Locate every Plasmodium parasite.
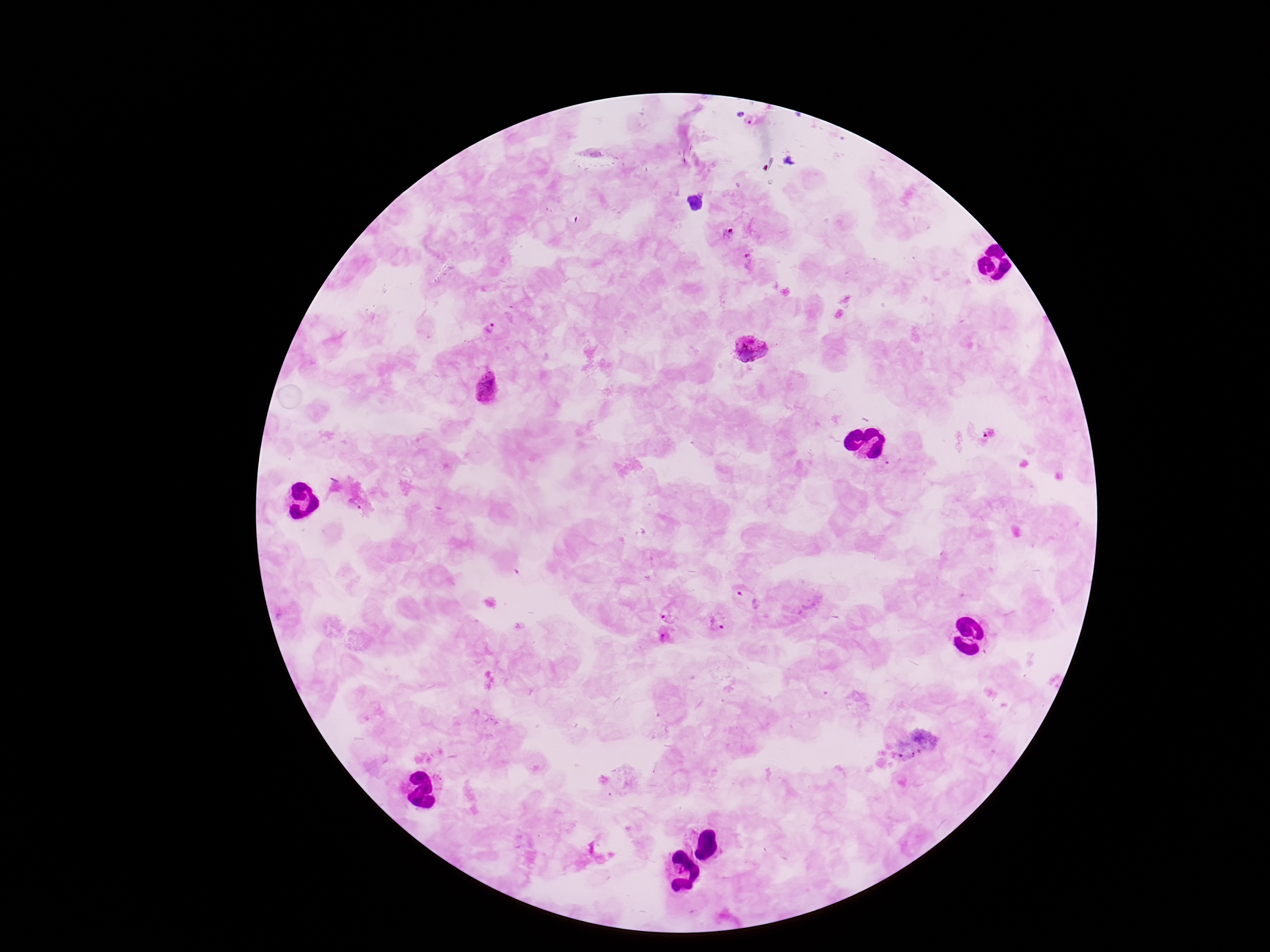

Approximate centers as (x, y) in pixels.
Plasmodium parasites: (756, 122), (726, 233), (751, 261), (488, 327), (749, 347), (488, 391), (988, 435), (355, 503), (749, 598), (670, 613), (717, 623), (665, 636).

Single field of view. Patient malaria status: infected. Giemsa stain. 100x magnification. Thick peripheral-blood smear. Photographed through the microscope eyepiece with a smartphone camera. Image is 1270×952 pixels.